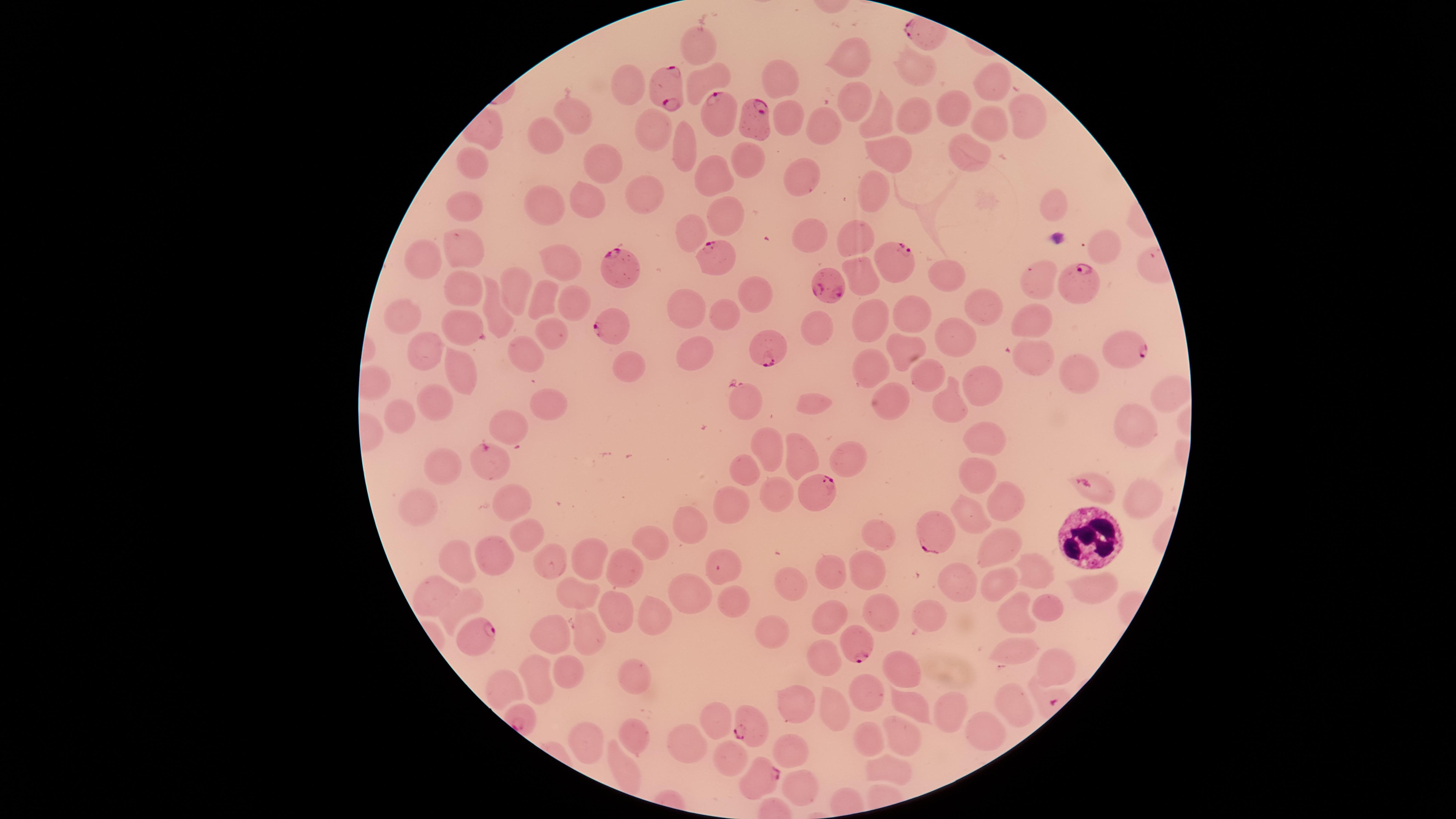

Approximate marker points as [x, y] in pixels.
Summary:
  - WBCs: [1090, 538]
  - Parasitized RBCs: [672, 82], [716, 112], [754, 124], [714, 254], [909, 265], [616, 267], [1082, 283], [831, 284], [611, 327], [1132, 344], [770, 348], [492, 461], [1090, 487], [818, 492], [936, 529], [719, 570], [474, 631], [855, 644], [746, 724], [758, 776]
  - Uninfected RBCs: [693, 46], [849, 55], [914, 65], [991, 75], [780, 79], [707, 80], [633, 81], [848, 99], [950, 106], [914, 113], [574, 114], [788, 118], [877, 119], [990, 122], [820, 127], [1022, 127], [652, 129], [544, 132], [680, 147], [888, 148], [973, 155], [594, 160], [746, 160], [472, 170], [708, 176], [799, 177], [640, 188], [873, 195], [466, 203], [585, 203], [547, 205], [1054, 205], [726, 217], [691, 230], [813, 234], [861, 239], [1103, 246], [461, 249], [419, 256], [557, 262], [866, 270], [949, 277], [1043, 277], [752, 287], [465, 289], [514, 292], [543, 295], [569, 298], [984, 306], [688, 309], [728, 311], [906, 312], [499, 313], [1033, 318], [402, 319], [866, 325], [816, 327], [462, 330], [553, 331], [958, 334], [905, 347], [419, 351], [1030, 351], [521, 352], [701, 356], [1076, 365], [455, 366], [628, 367], [879, 370], [930, 375], [985, 384], [1163, 391], [439, 397], [892, 398], [742, 401], [813, 403], [547, 404], [403, 405], [952, 406], [507, 420], [1137, 424], [985, 430], [770, 441], [805, 452], [844, 454], [742, 459], [442, 462], [975, 475], [773, 494], [1142, 500], [732, 502], [517, 504], [999, 505], [416, 506], [965, 514], [690, 521], [525, 534], [878, 537], [654, 539], [996, 546], [491, 552], [590, 556], [458, 558], [621, 561], [550, 562], [1024, 564], [832, 569], [865, 569], [796, 575], [993, 583], [953, 585], [438, 586], [688, 587], [1089, 587], [573, 596], [466, 600], [731, 600], [1046, 606], [620, 607], [820, 611], [872, 611], [1017, 612], [657, 613], [927, 618], [581, 631], [552, 633], [772, 633], [1015, 643], [823, 649], [905, 664], [1054, 666], [566, 675], [537, 677], [633, 678], [503, 686], [870, 690], [797, 696], [908, 700], [1012, 702], [954, 707], [829, 717], [716, 719], [986, 730], [629, 733], [586, 738], [902, 738], [870, 740], [684, 742], [791, 746], [728, 758], [887, 770], [800, 787]
  - Species: Plasmodium falciparum
  - Preparation: thin smear of blood
  - Presence: malaria parasites detected
  - Image size: 1456×819 pixels
  - Stain: Giemsa
  - Field of view: single
  - Capture: smartphone photograph through the microscope eyepiece
  - Visible region: circular